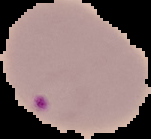

preparation = thin blood film
result = Plasmodium parasites detected
image size = 151×139 pixels
image type = segmented cell region on a black background